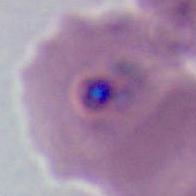

modality = micrograph
magnification = 400x or 1000x
identification = Plasmodium